Describe the morphology of the red blood cells.
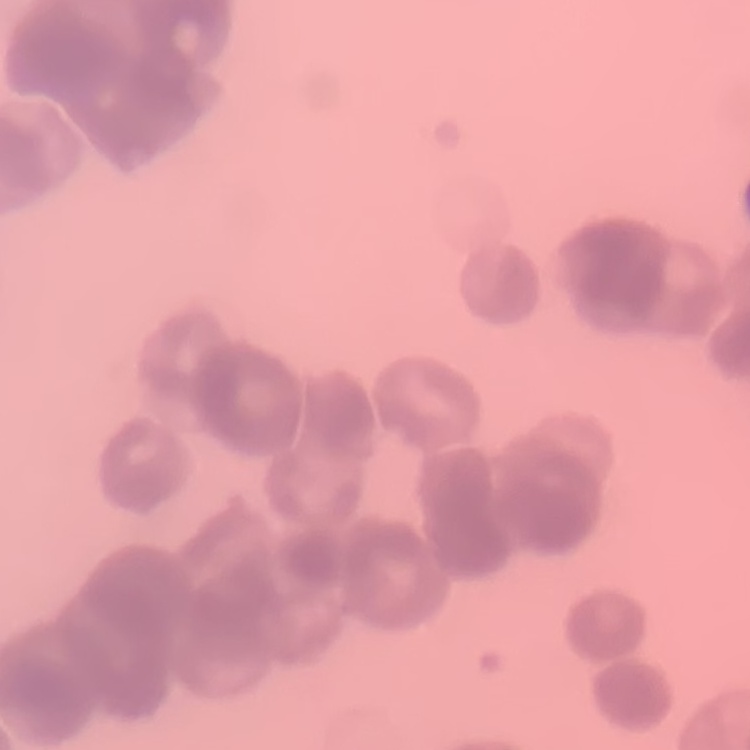

They show rouleaux formation.

Thin blood smear. One tile cut from a larger photomicrograph. Field's or Giemsa stain.